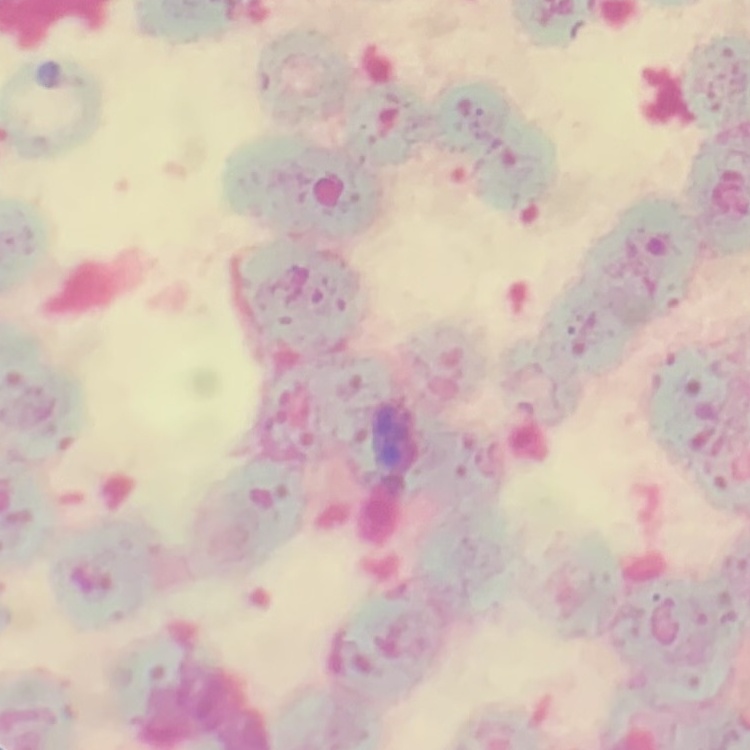

Summary:
  - Erythrocyte morphology: rouleaux formation
  - Image type: one tile cut from a larger photomicrograph
  - Preparation: thin peripheral smear
  - Stain: Field's or Giemsa